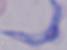
A trypanosome is seen. 1000x magnification. Photomicrograph.